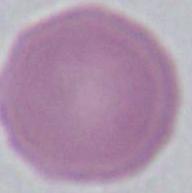
An erythrocyte is shown. Captured at 1000x magnification. Photomicrograph.